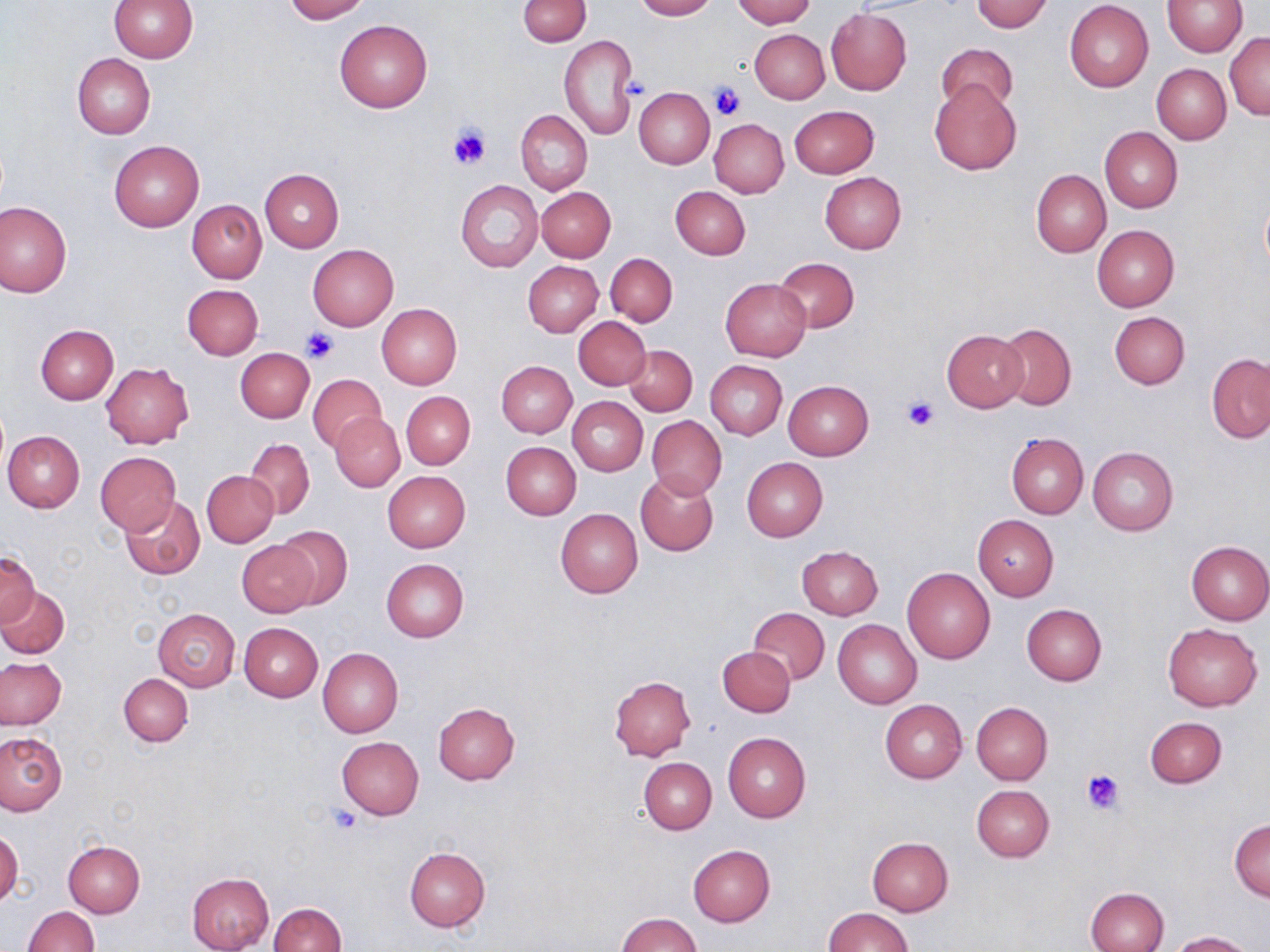 Approximate bounding boxes as (x1, y1, x2, y2) in pixels. Platelet locations: (626, 78, 652, 100), (707, 81, 747, 121), (450, 125, 492, 170), (302, 328, 338, 364), (902, 396, 941, 432), (1082, 768, 1126, 812), (326, 805, 364, 836). Uninfected red blood cell locations: (109, 0, 197, 62), (282, 0, 369, 22), (517, 0, 591, 47), (631, 0, 715, 20), (731, 0, 815, 27), (1162, 0, 1245, 57), (971, 1, 1053, 32), (1065, 1, 1153, 91), (826, 8, 911, 95), (334, 19, 432, 113), (750, 29, 829, 104), (1225, 33, 1270, 119), (559, 36, 637, 139), (937, 39, 1019, 117), (72, 53, 156, 137), (1152, 64, 1231, 143), (930, 79, 1022, 175), (634, 87, 714, 170), (788, 105, 879, 178), (515, 110, 591, 194), (710, 118, 789, 197), (1099, 127, 1182, 213), (108, 140, 203, 231), (260, 168, 343, 251), (1031, 169, 1111, 258), (820, 172, 906, 254), (455, 180, 542, 272), (671, 185, 750, 259), (537, 187, 616, 262), (187, 200, 267, 283), (0, 202, 71, 297), (1092, 225, 1180, 312), (307, 244, 398, 332), (605, 253, 677, 327), (773, 257, 859, 333), (523, 261, 603, 337), (720, 279, 810, 362), (183, 284, 263, 359), (196, 296, 283, 399), (376, 303, 462, 389), (1109, 311, 1189, 389), (573, 316, 651, 390), (996, 322, 1076, 411), (36, 324, 118, 404), (943, 330, 1029, 412), (624, 344, 698, 416), (235, 347, 314, 422), (1207, 354, 1270, 443), (705, 360, 787, 440), (497, 361, 576, 438), (101, 362, 193, 449), (308, 373, 387, 452), (783, 380, 874, 460), (402, 391, 474, 469), (567, 396, 647, 476), (330, 411, 404, 492), (647, 416, 727, 498), (3, 431, 83, 512), (1006, 433, 1088, 518), (245, 438, 315, 519), (502, 442, 581, 520), (1087, 447, 1177, 536), (95, 451, 180, 535), (742, 457, 828, 541), (203, 469, 279, 546), (382, 471, 470, 551), (636, 472, 719, 555), (120, 495, 205, 578), (556, 509, 644, 598), (973, 516, 1059, 600), (275, 526, 353, 610), (237, 540, 318, 616), (1185, 540, 1270, 624), (797, 547, 882, 620), (1, 552, 40, 629), (381, 559, 469, 642), (903, 568, 995, 664), (0, 585, 70, 658), (1021, 604, 1107, 686), (750, 608, 829, 684), (152, 609, 239, 691), (833, 620, 921, 708), (240, 623, 323, 701), (1162, 624, 1262, 711), (718, 645, 795, 717), (318, 648, 402, 737), (1, 658, 66, 729), (119, 673, 192, 747), (609, 675, 696, 761), (880, 699, 967, 783), (972, 701, 1052, 784), (433, 702, 520, 784), (1144, 716, 1227, 788), (0, 732, 66, 815), (723, 732, 810, 822), (336, 737, 424, 819), (638, 757, 716, 834), (971, 785, 1054, 861), (1229, 818, 1269, 901), (0, 827, 23, 909), (865, 837, 953, 916), (63, 840, 145, 917), (688, 844, 776, 926), (405, 847, 490, 931), (186, 872, 275, 952), (1086, 886, 1169, 952), (268, 902, 346, 952), (22, 906, 99, 952), (822, 907, 913, 951), (615, 913, 704, 952), (1166, 930, 1255, 951). Slide-level diagnosis: no evidence of blood parasites. May-Grünwald-Giemsa-stained preparation. Thin blood smear. Image is 1270×952 pixels. Captured at 1000x magnification. Optical microscopy. Single field of view.